Report the malaria status of this cell.
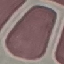

Uninfected.

{
  "image_type": "cell patch, automatically extracted from a larger field of view and resized to 64 × 64 pixels",
  "preparation": "thin blood smear",
  "capture": "smartphone camera at the microscope eyepiece",
  "stain": "Giemsa"
}